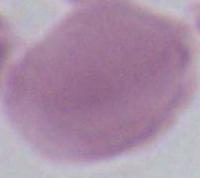

Summary:
  - Identification: erythrocyte
  - Modality: photomicrograph
  - Magnification: 1000x